Assess this cell for malaria.
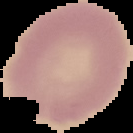

It is uninfected.

Summary:
  - Image size: 133×133 pixels
  - Image type: segmented cell region with the area outside set to black
  - Preparation: thin blood smear